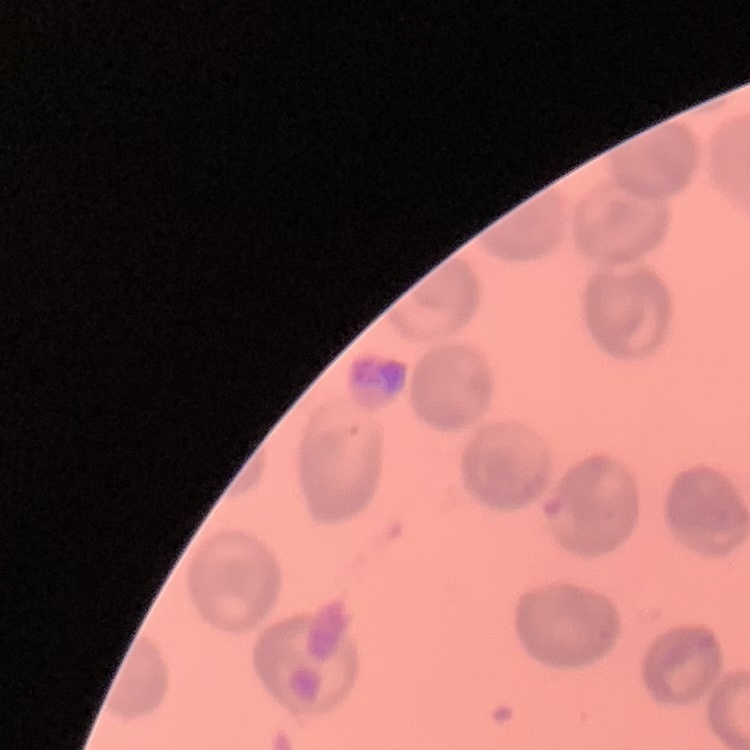 The erythrocytes show no rouleaux formation. Square crop of a larger photomicrograph. Stained with either Field's or Giemsa. Thin blood film.